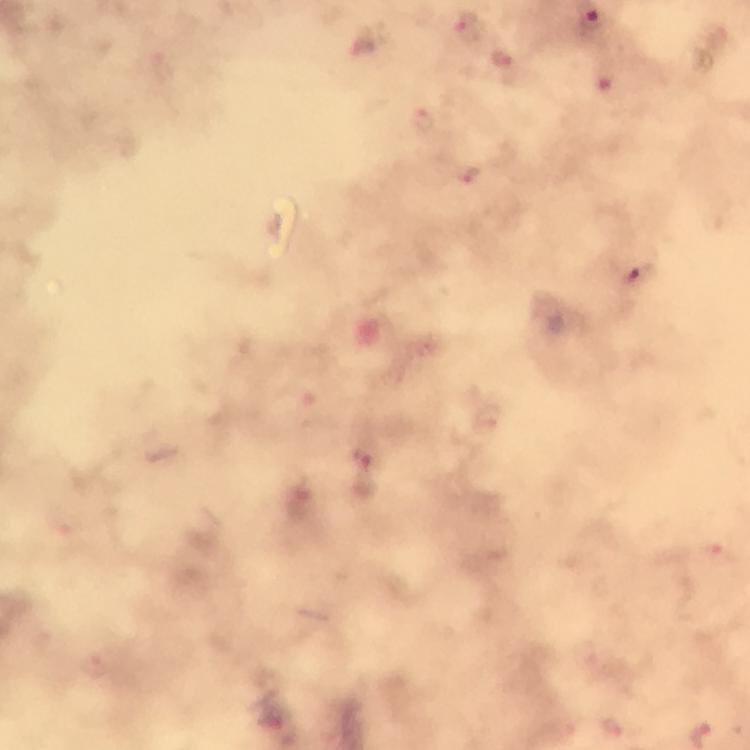

Approximate centers as {x, y} in pixels.
Summary:
  - Plasmodium parasite locations: {465, 21}, {593, 21}, {501, 62}, {609, 78}, {420, 120}, {469, 175}, {636, 281}, {362, 472}
  - Image size: 750×750 pixels
  - Preparation: thick blood film
  - Capture: smartphone camera through the microscope
  - Context: from a malaria diagnostic workup
  - Stain: Giemsa
  - Immersion oil: applied
  - Cropped from: a single field of view
  - Magnification: 100x